Assess this cell for malaria.
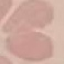

It is uninfected.

Thin smear of blood. Cell patch, automatically extracted from a larger field of view and resized to 64 × 64 pixels. Acquired by smartphone through the microscope eyepiece. Giemsa stain.